Report the malaria status of this cell.
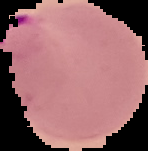

It is parasitized.

image type = segmented cell region with the area outside set to black
image size = 148×151 pixels
preparation = thin blood film